Name the blood parasite species.
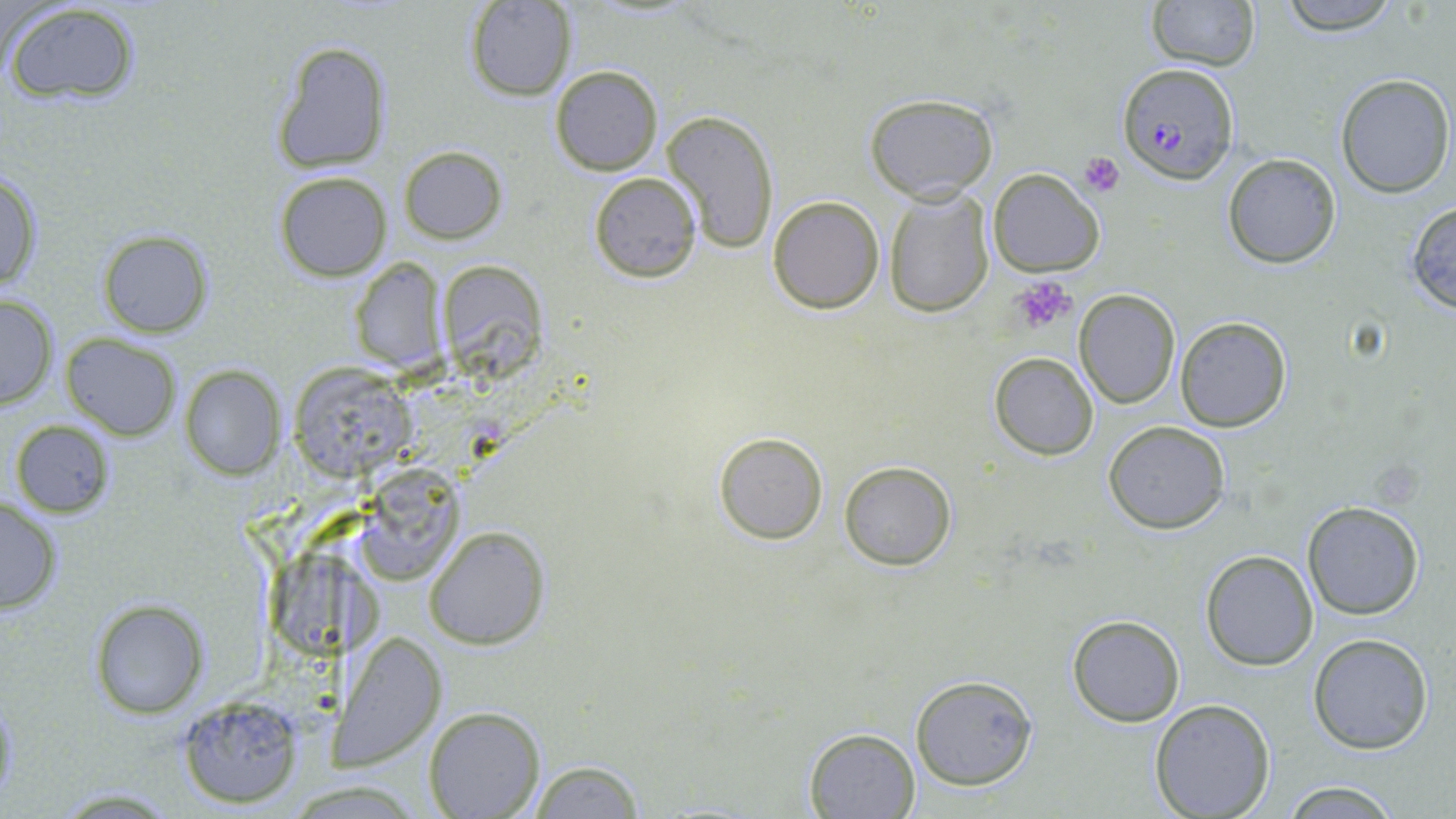
Plasmodium falciparum.

Approximate bounding boxes as (x1,y1)-(x2,y2) corner pairs in pixels. Plasmodium falciparum-infected red blood cell locations: (1118,62)-(1238,185). Platelet locations: (1078,152)-(1125,196), (1012,279)-(1075,334). Uninfected red blood cell locations: (1147,0)-(1260,71), (1274,0)-(1403,34), (2,1)-(143,104), (465,1)-(575,101), (271,39)-(392,176), (550,64)-(663,174), (1335,74)-(1454,196), (866,93)-(999,203), (661,108)-(781,255), (400,145)-(506,244), (1222,154)-(1342,268), (988,168)-(1105,277), (0,171)-(44,295), (274,171)-(392,281), (589,172)-(702,282), (882,190)-(995,317), (767,195)-(885,314), (1405,199)-(1456,313), (96,229)-(214,337), (349,257)-(446,374), (1075,289)-(1179,409), (0,292)-(59,411), (1174,316)-(1291,433), (61,333)-(183,441), (989,352)-(1098,461), (180,366)-(285,478), (289,366)-(413,477), (10,419)-(116,517), (1103,421)-(1231,534), (713,430)-(830,545), (840,461)-(956,569), (357,464)-(464,585), (0,498)-(62,613), (1302,500)-(1426,620), (424,528)-(549,649), (1200,549)-(1319,672), (267,553)-(381,655), (89,601)-(205,718), (1066,614)-(1186,728), (338,633)-(448,768), (1307,633)-(1434,754), (910,674)-(1039,790), (174,694)-(308,808), (1149,698)-(1277,819), (423,706)-(544,817), (804,727)-(920,817), (525,759)-(646,819), (1275,778)-(1407,817). Thin blood smear. May-Grünwald-Giemsa-stained preparation. Optical microscopy. One field of a larger specimen. Image is 1456×819 pixels. 1000x magnification.